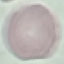

Result: no malaria parasites seen. Photographed with a smartphone camera at the microscope eyepiece. Giemsa stain. Automatically extracted cell patch, resized to 64 × 64 pixels. Thin blood film.